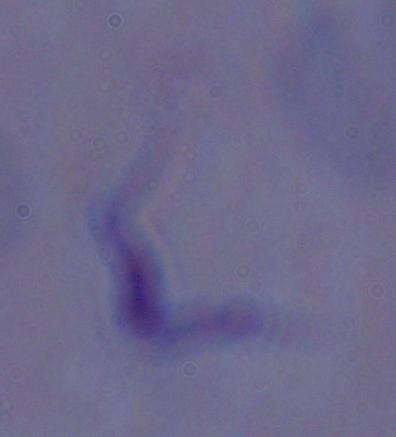
Summary:
  - Modality: photomicrograph
  - Magnification: 1000x
  - Identification: trypanosome